Assess this cell for malaria.
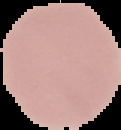

Uninfected.

{
  "image_type": "cell region segmented out of the field of view; surrounding area masked to black",
  "preparation": "thin blood film",
  "image_size": "121×130 pixels"
}